Assess the morphology of the red blood cells.
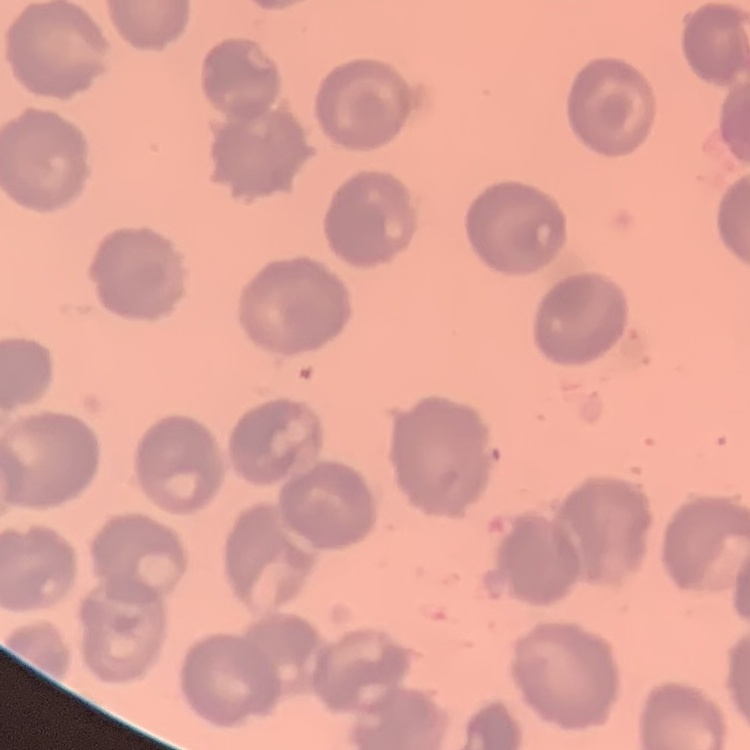
They show no rouleaux formation.

Thin blood smear. One tile cut from a larger photomicrograph. Field's or Giemsa stain.